Report the malaria status of this cell.
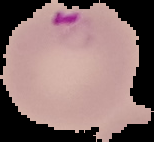
It is parasitized.

Segmented cell region on a black background. Image is 154×142 pixels. From a thin blood film.